Give the position of every Plasmodium parasite.
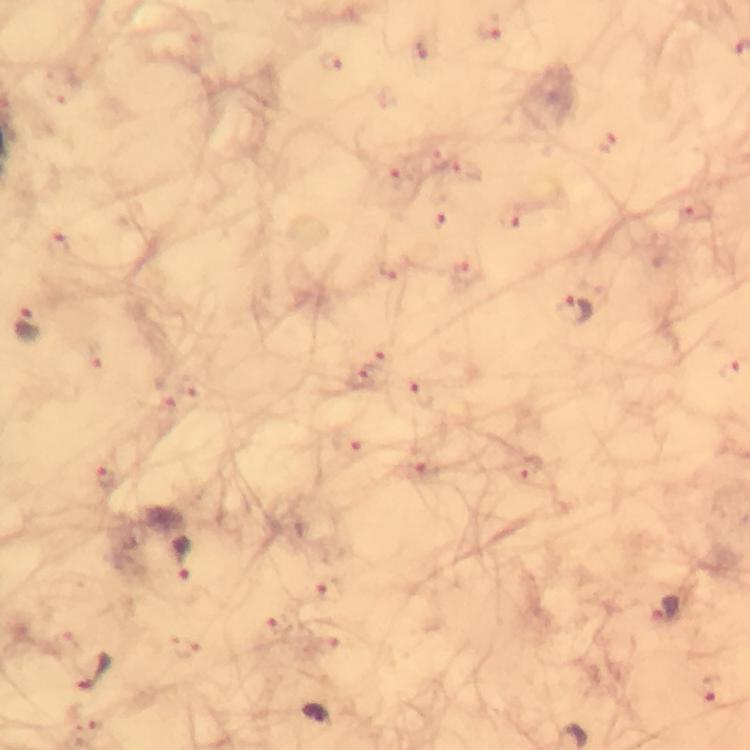

Approximate object centers, in pixels from the top-left corner.
Plasmodium parasites: (x=574, y=311), (x=27, y=325), (x=184, y=559), (x=664, y=610), (x=95, y=674), (x=312, y=715).

{
  "preparation": "thick blood film",
  "context": "from a malaria diagnostic workup",
  "magnification": "100x",
  "stain": "Giemsa",
  "immersion_oil": "used",
  "cropped_from": "one field of view",
  "image_size": "750×750 pixels",
  "capture": "smartphone mounted on the microscope"
}